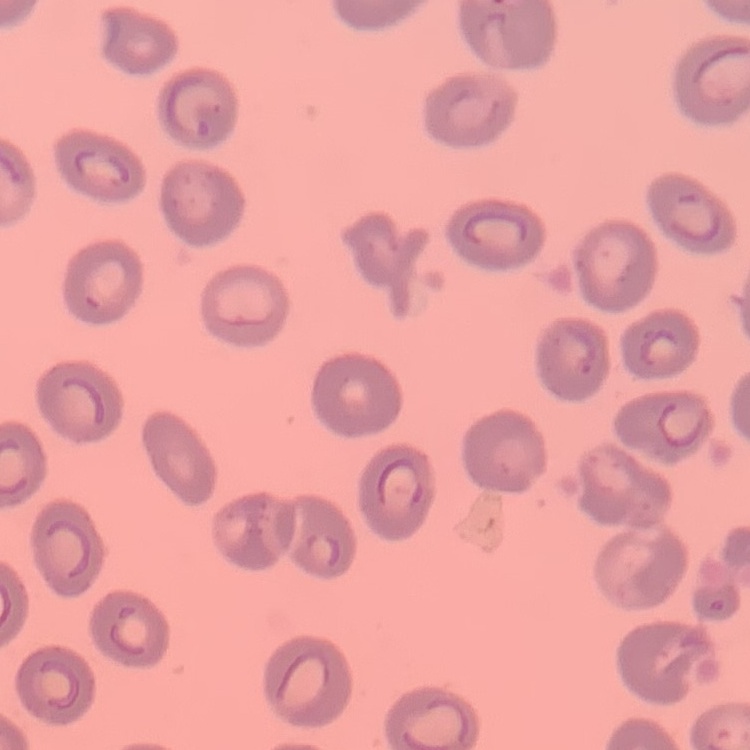
red_blood_cell_morphology: no rouleaux formation
image_type: square crop of a larger photomicrograph
stain: Field's or Giemsa
preparation: thin blood smear